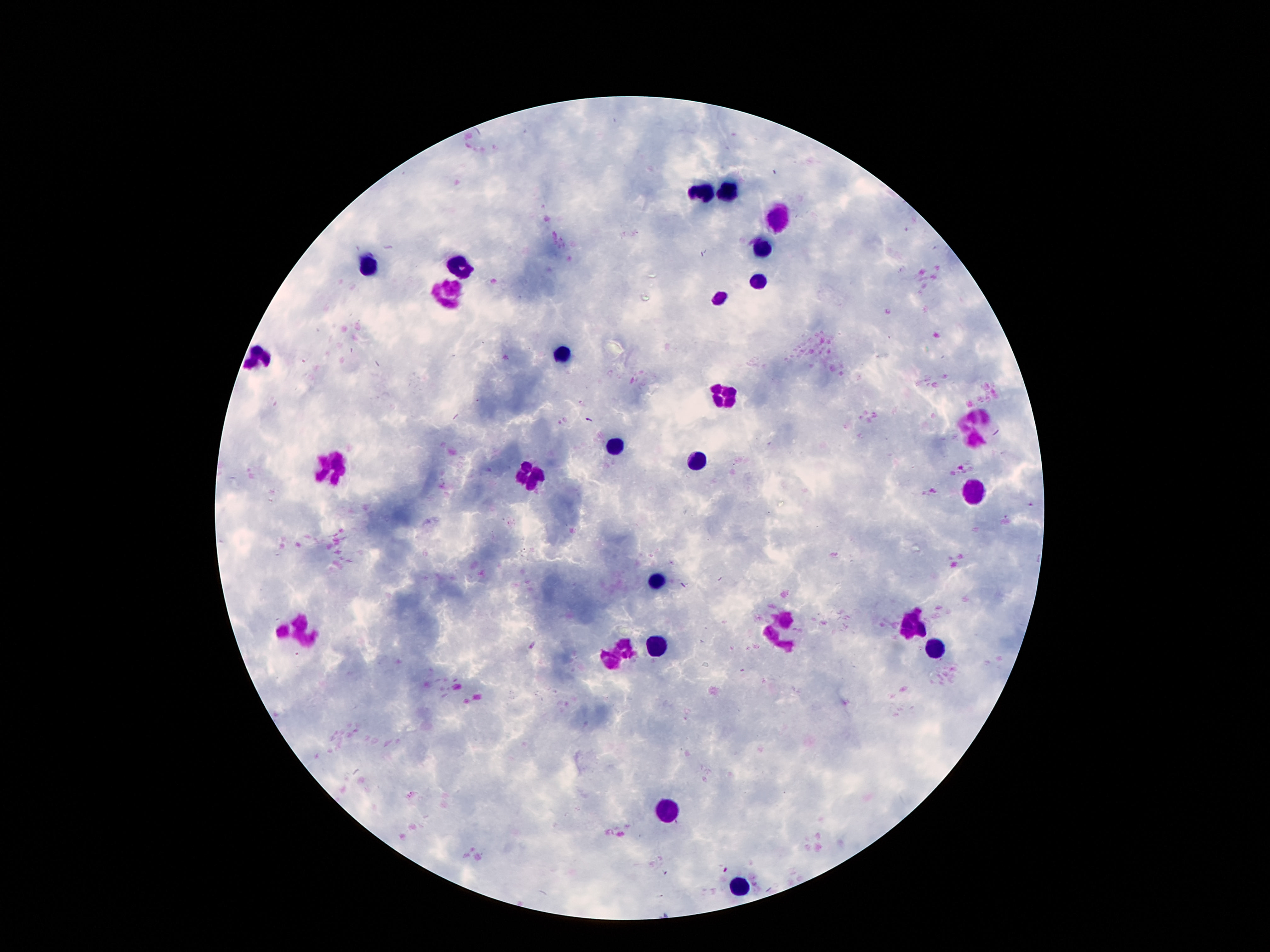

preparation: thick blood film
image_size: 1270×952 pixels
stain: Giemsa
leukocyte_locations: 'approximate centers as [x, y] in pixels: [702, 191], [730, 191], [774, 217], [760, 251], [366, 264], [462, 271], [756, 282], [450, 292], [718, 298], [261, 355], [564, 357], [723, 391], [973, 429], [613, 445], [697, 457], [333, 462], [527, 478], [971, 488], [651, 581], [910, 623], [777, 630], [298, 634], [940, 646], [653, 649], [616, 658], [672, 809], [739, 885]'
patient_malaria_status: not infected
field_of_view: single
magnification: 100x
capture: smartphone camera through the microscope eyepiece